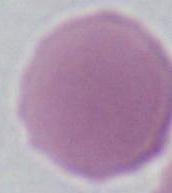
Summary:
  - Modality: micrograph
  - Magnification: 1000x
  - Identification: erythrocyte